Comment on the morphology of the red blood cells.
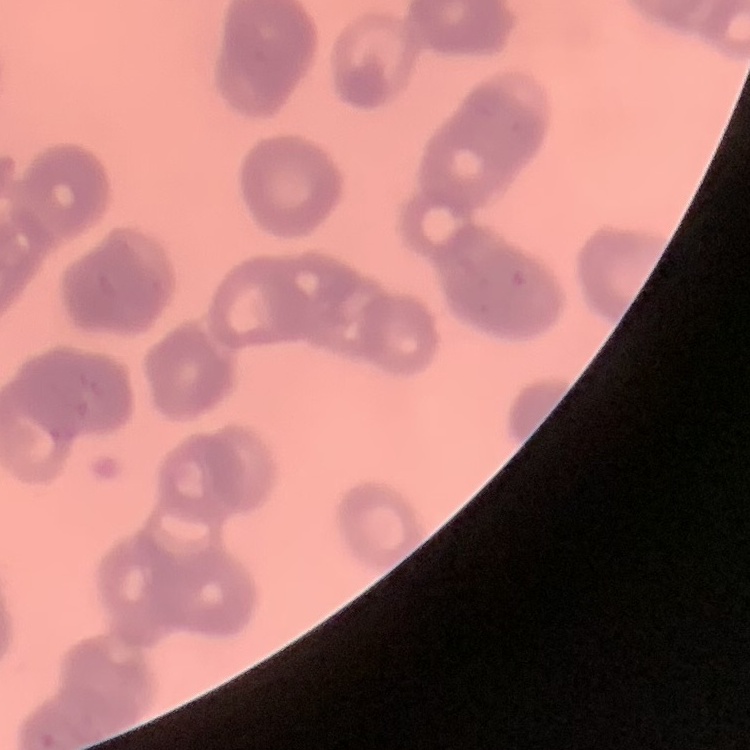
They show rouleaux formation.

Thin blood film. Stained with either Field's or Giemsa. Square crop of a larger photomicrograph.